Locate and identify every blood parasite.
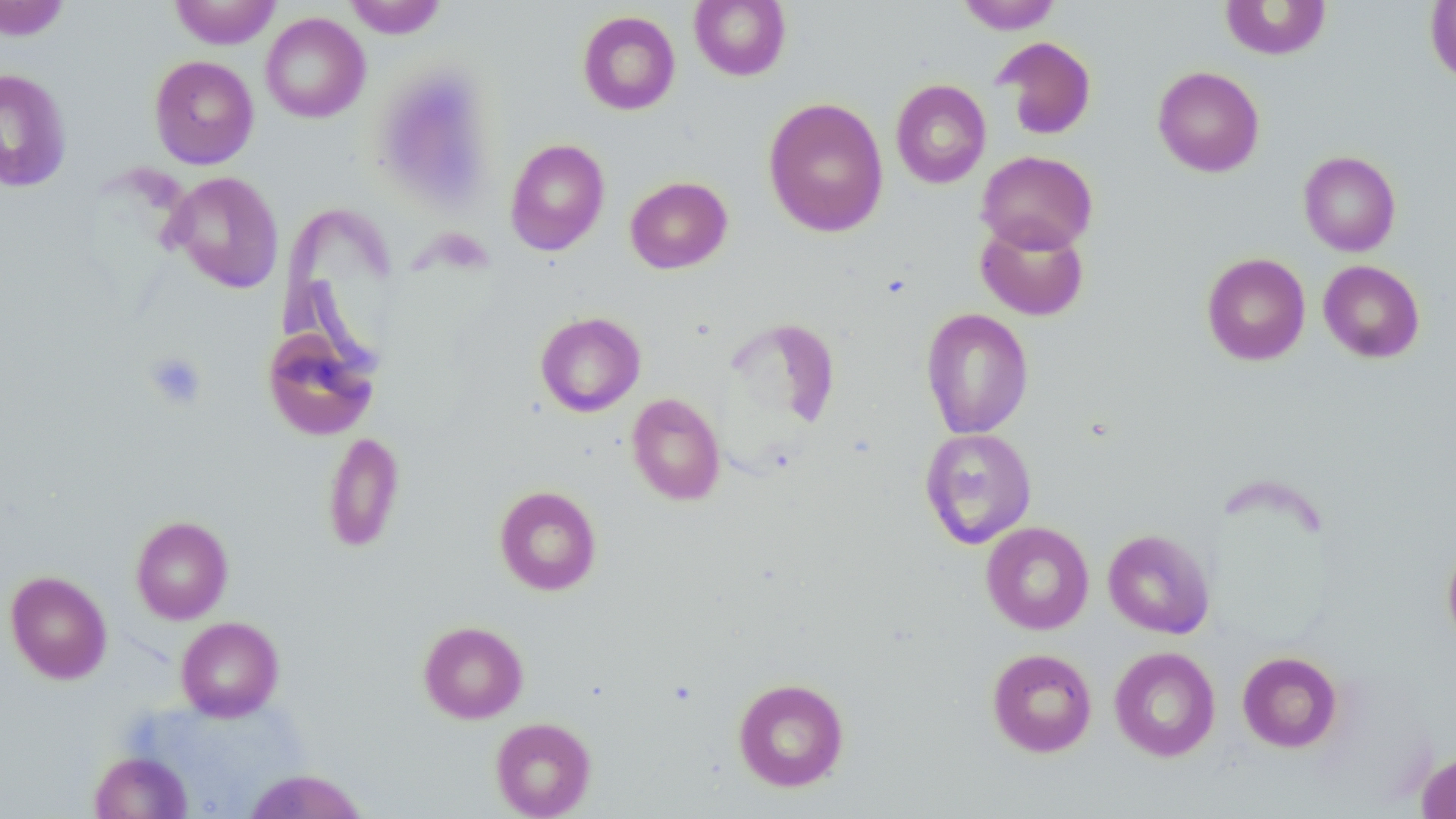
No blood parasites observed.

Approximate bounding boxes as (x1,y1)-(x2,y2) corner pairs in pixels. Uninfected red blood cell locations: (1,0)-(70,41), (169,0)-(281,49), (343,0)-(448,39), (689,0)-(791,81), (957,0)-(1062,33), (1219,0)-(1333,60), (1425,0)-(1456,85), (577,10)-(681,115), (260,13)-(370,123), (992,36)-(1097,140), (149,55)-(259,169), (1153,66)-(1264,177), (0,68)-(72,194), (891,79)-(991,188), (762,97)-(889,237), (505,138)-(609,256), (976,150)-(1098,254), (1298,150)-(1401,256), (166,171)-(284,293), (625,176)-(733,274), (975,218)-(1090,321), (1201,252)-(1310,366), (1318,260)-(1425,363), (920,308)-(1034,439), (535,311)-(646,417), (262,326)-(380,441), (627,393)-(726,505), (919,427)-(1037,549), (322,431)-(405,553), (494,485)-(602,596), (130,515)-(234,623), (981,522)-(1094,634), (1102,528)-(1216,638), (1442,535)-(1456,650), (5,570)-(112,684), (175,616)-(284,721), (418,620)-(528,723), (1109,646)-(1221,761), (986,648)-(1097,757), (1237,651)-(1343,753), (732,677)-(849,792), (490,717)-(596,818), (1415,749)-(1456,819), (90,751)-(193,818), (243,769)-(369,818). Platelet locations: (144,352)-(206,410). Slide-level diagnosis: no evidence of blood parasites. Image is 1456×819 pixels. Thin blood smear. May-Grünwald-Giemsa stain. Captured at 1000x magnification. Single field of view. Light microscopy.